Classify this cell by malaria status.
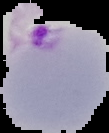

It is parasitized.

preparation = thin blood film
image type = cell region segmented out of the field of view; surrounding area masked to black
image size = 109×133 pixels